Assess this cell for malaria.
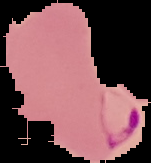

It is parasitized.

Summary:
  - Preparation: thin blood film
  - Image size: 151×163 pixels
  - Image type: segmented cell region on a black background